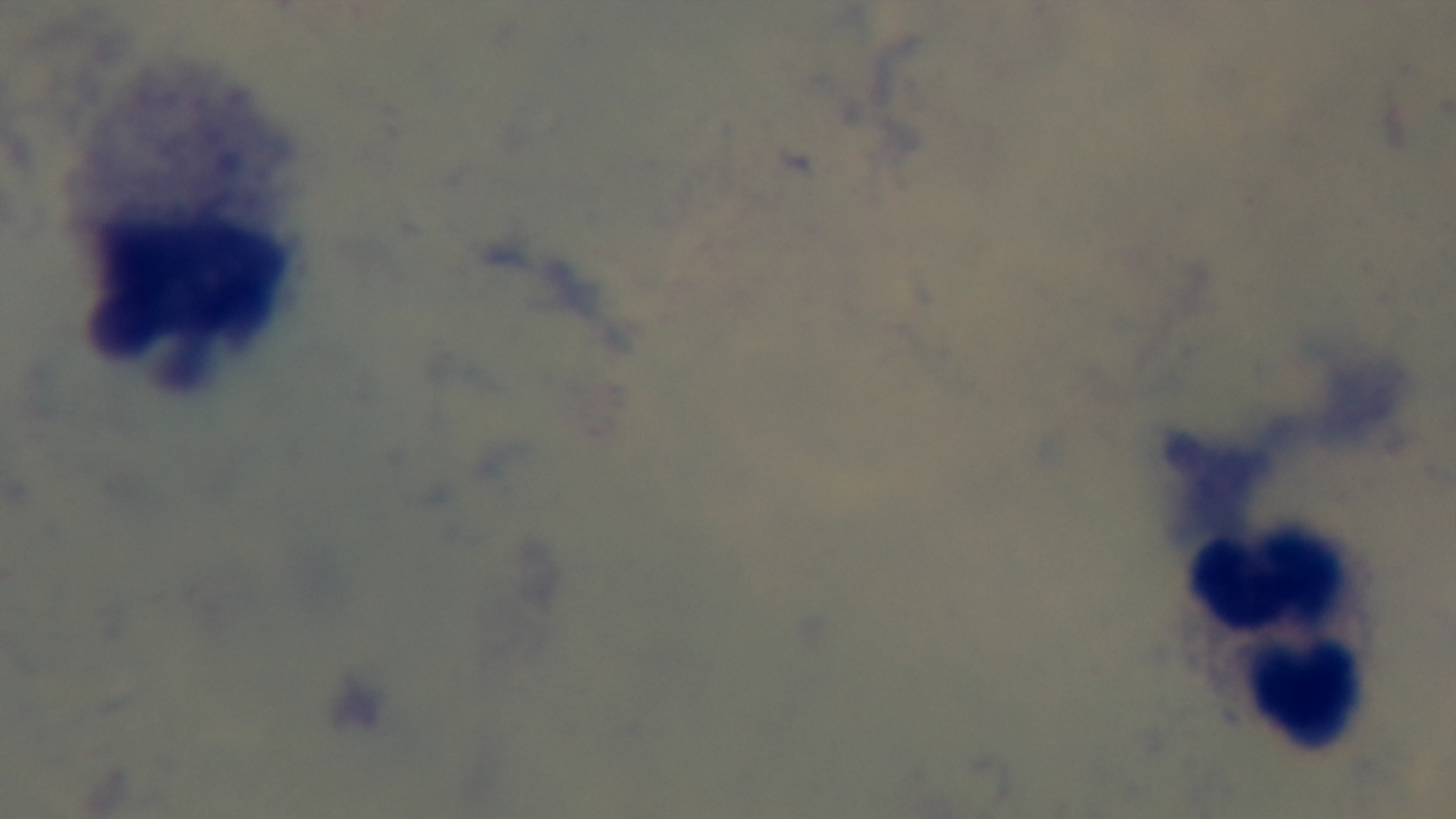
preparation = thick blood film
malaria status = uninfected
stain = Giemsa
objective = 100x oil immersion
field of view = single
capture = mounted 4K digital camera
modality = light microscopy